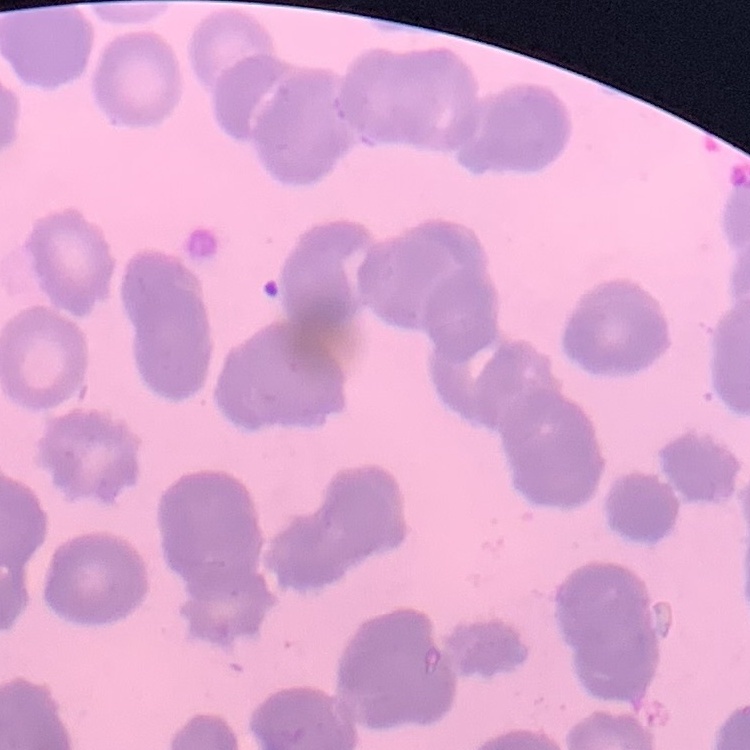
Summary:
  - Red blood cell morphology: rouleaux formation
  - Image type: square crop of a larger photomicrograph
  - Preparation: thin blood smear
  - Stain: Field's or Giemsa